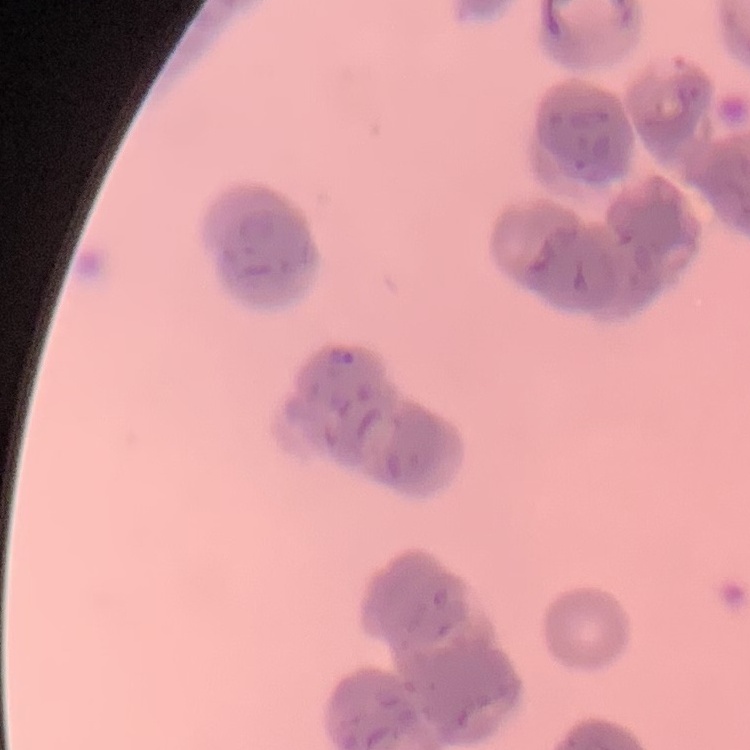
erythrocyte_morphology: rouleaux formation
image_type: square crop of a larger photomicrograph
preparation: thin blood smear
stain: Field's or Giemsa